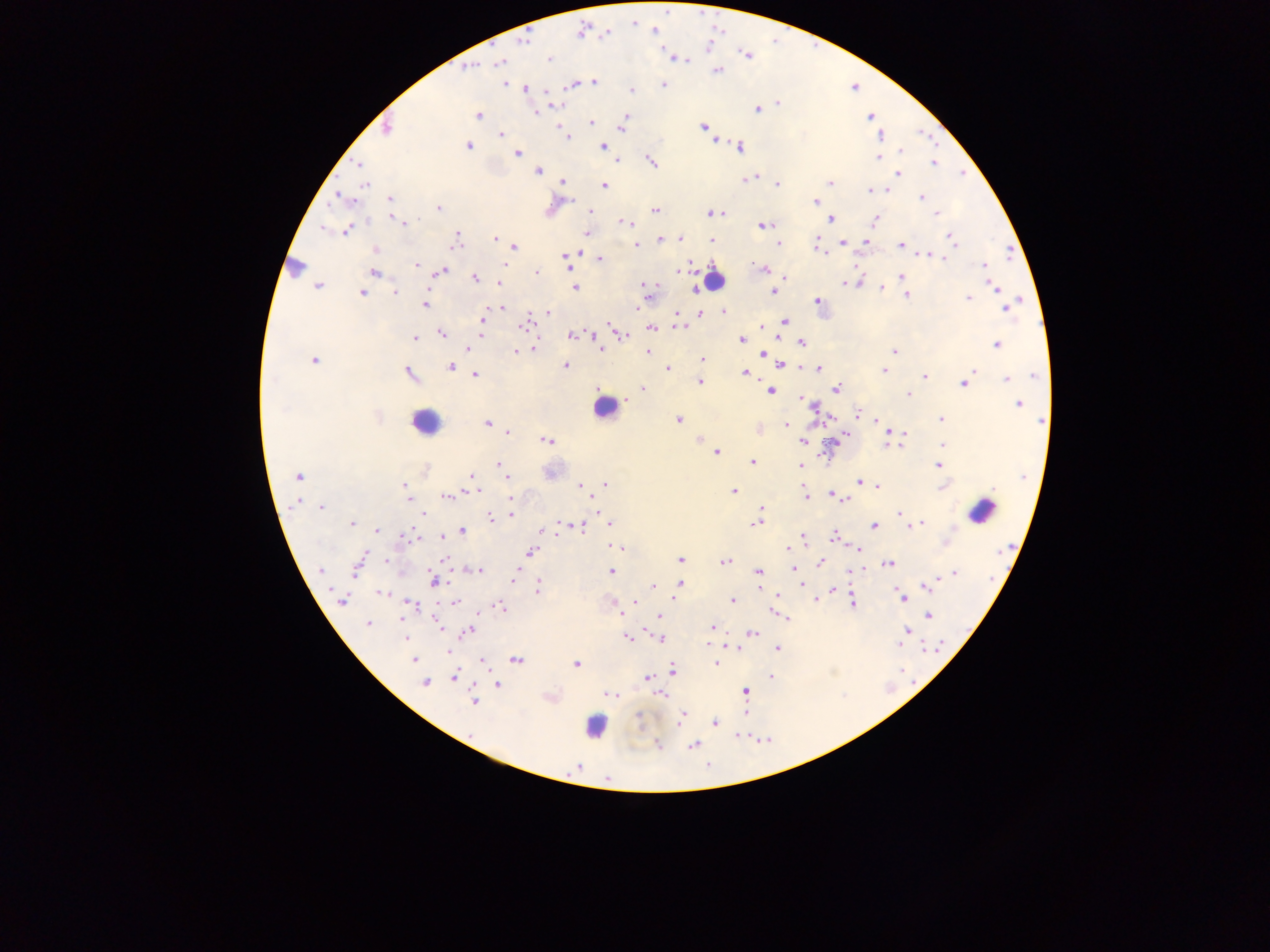

Approximate centers as [x, y] in pixels. Plasmodium parasite locations: [633, 22], [582, 32], [607, 32], [523, 41], [746, 56], [674, 57], [549, 59], [499, 63], [469, 67], [716, 70], [594, 82], [503, 84], [663, 84], [572, 85], [525, 88], [630, 91], [547, 94], [776, 102], [552, 106], [757, 108], [535, 113], [478, 115], [869, 117], [624, 120], [590, 123], [559, 125], [622, 126], [386, 127], [704, 127], [501, 134], [881, 135], [566, 138], [715, 139], [468, 146], [603, 146], [739, 147], [901, 150], [516, 153], [877, 156], [615, 160], [651, 161], [359, 163], [932, 163], [537, 170], [898, 172], [753, 177], [746, 179], [562, 181], [777, 183], [830, 183], [365, 184], [605, 186], [869, 190], [337, 195], [921, 197], [390, 199], [814, 202], [439, 208], [655, 210], [590, 211], [723, 212], [711, 213], [935, 213], [395, 219], [829, 219], [875, 220], [623, 221], [403, 223], [762, 225], [347, 229], [586, 233], [950, 236], [456, 237], [495, 239], [660, 239], [679, 239], [816, 239], [711, 240], [843, 242], [867, 242], [454, 243], [778, 243], [636, 244], [816, 244], [901, 246], [514, 247], [819, 249], [376, 250], [928, 253], [938, 255], [566, 258], [600, 258], [415, 264], [567, 265], [751, 265], [504, 266], [984, 266], [758, 268], [764, 269], [441, 271], [373, 272], [678, 272], [535, 273], [901, 276], [475, 277], [785, 277], [641, 283], [845, 283], [858, 283], [645, 284], [317, 285], [994, 287], [575, 288], [695, 288], [882, 288], [395, 291], [773, 291], [999, 291], [361, 292], [648, 293], [907, 295], [968, 297], [818, 301], [424, 304], [503, 306], [1006, 307], [639, 309], [724, 311], [548, 312], [700, 313], [676, 316], [482, 319], [784, 321], [524, 323], [679, 326], [761, 327], [650, 328], [615, 329], [441, 333], [570, 335], [481, 336], [623, 336], [414, 338], [741, 339], [801, 343], [995, 343], [600, 347], [467, 348], [535, 348], [763, 351], [894, 351], [516, 352], [647, 352], [312, 359], [701, 360], [781, 364], [565, 365], [450, 366], [667, 368], [800, 368], [819, 368], [972, 369], [883, 370], [744, 372], [409, 374], [476, 375], [924, 376], [1033, 376], [1006, 377], [700, 382], [964, 383], [642, 388], [835, 388], [769, 391], [908, 393], [799, 399], [1017, 402], [812, 406], [856, 412], [376, 418], [678, 419], [940, 419], [1042, 420], [486, 423], [785, 425], [757, 429], [507, 431], [846, 432], [889, 434], [902, 434], [700, 438], [547, 440], [802, 441], [886, 442], [942, 445], [900, 446], [716, 451], [752, 462], [498, 464], [938, 465], [800, 466], [471, 475], [298, 477], [506, 477], [859, 480], [606, 484], [403, 485], [580, 486], [941, 486], [876, 487], [476, 489], [470, 491], [733, 491], [405, 492], [831, 494], [805, 495], [447, 496], [511, 496], [845, 497], [409, 501], [594, 503], [321, 507], [424, 513], [899, 513], [510, 514], [490, 517], [561, 522], [607, 522], [755, 522], [921, 522], [351, 523], [874, 525], [581, 526], [909, 526], [377, 529], [462, 530], [542, 530], [442, 536], [802, 536], [835, 537], [946, 542], [609, 544], [620, 548], [858, 548], [787, 550], [530, 552], [444, 558], [680, 559], [386, 560], [726, 561], [820, 562], [888, 563], [358, 565], [793, 568], [320, 570], [479, 570], [611, 571], [758, 572], [515, 573], [955, 574], [434, 580], [514, 581], [801, 583], [680, 584], [653, 585], [927, 586], [537, 588], [757, 589], [832, 590], [381, 592], [777, 594], [902, 597], [813, 599], [341, 600], [634, 600], [732, 600], [455, 602], [411, 603], [852, 603], [500, 606], [773, 612], [622, 615], [927, 615], [659, 617], [787, 618], [402, 620], [367, 624], [442, 628], [712, 628], [646, 629], [906, 630], [467, 632], [751, 633], [406, 638], [627, 638], [661, 639], [900, 644], [729, 646], [776, 648], [449, 650], [415, 659], [516, 659], [480, 662], [716, 662], [575, 664], [671, 669], [453, 676], [770, 676], [646, 679], [425, 683], [496, 684], [744, 692], [611, 693], [661, 694], [473, 701], [682, 714], [681, 719], [715, 723], [679, 725], [471, 734], [657, 744], [693, 745], [576, 766]. Leukocyte locations: [297, 266], [713, 279], [603, 408], [424, 422], [981, 511], [596, 726]. Mobile-phone photograph taken through the microscope. Image is 1270×952 pixels. Thick blood film. Single field of view. Collected in Ghana.